Assess this cell for malaria.
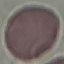
Uninfected.

preparation = thin blood smear
capture = smartphone through the microscope eyepiece
stain = Giemsa
image type = automatically extracted cell patch, resized to 64 × 64 pixels